Identify the parasite.
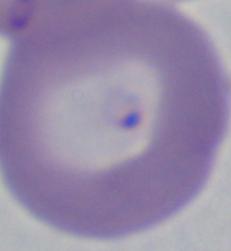
This is Babesia.

Summary:
  - Magnification: 1000x
  - Modality: micrograph